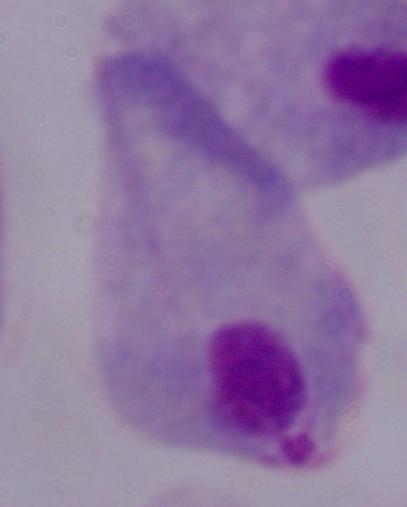
identification = trichomonad
magnification = 1000x
modality = micrograph